Locate every malaria parasite.
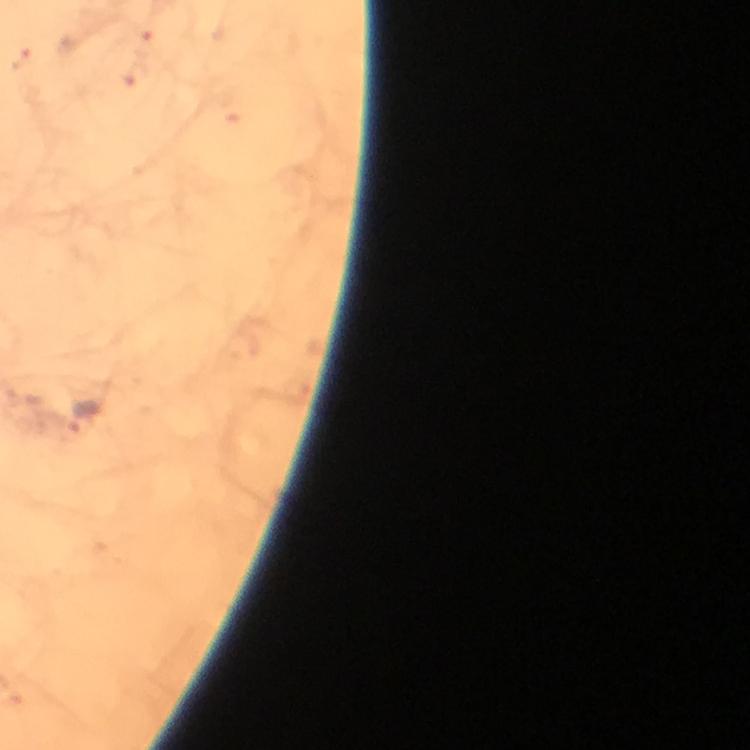

Approximate centers as [x, y] in pixels.
Malaria parasites: [83, 416].

From a diagnostic examination for malaria. Photographed through the microscope with a smartphone camera. Giemsa stain. Thick blood film. A crop from one field of view. Image is 750×750 pixels. Immersion oil applied. 100x magnification.